Identify the cell.
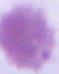

An erythrocyte.

1000x magnification. Photomicrograph.